Give the location of every parasitized red blood cell.
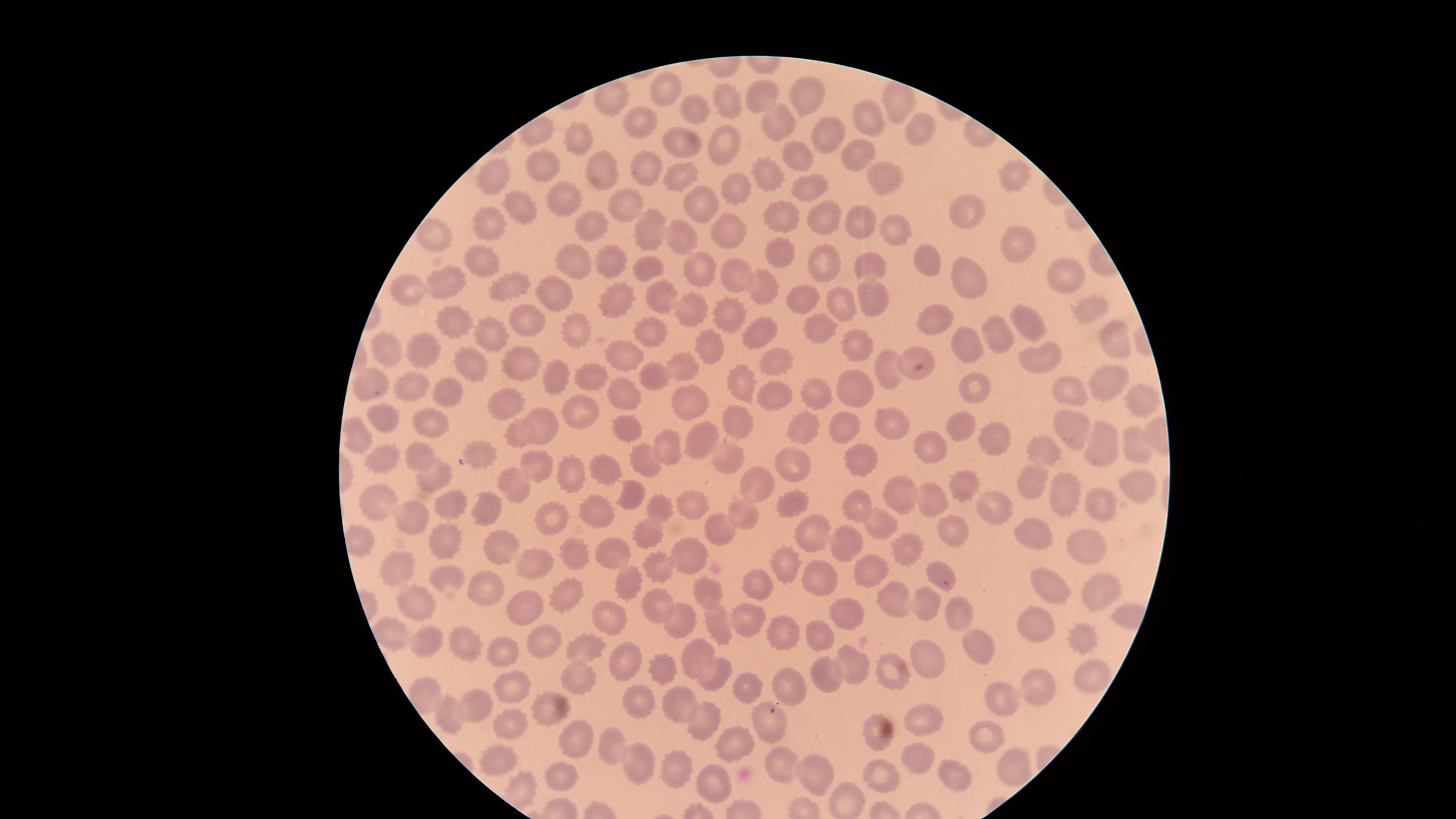
No parasitized red blood cells identified.

Approximate marker points, in pixels from the top-left corner.
Summary:
  - Uninfected red blood cells: (x=663, y=89), (x=763, y=95), (x=812, y=96), (x=726, y=101), (x=897, y=102), (x=697, y=104), (x=640, y=119), (x=869, y=119), (x=772, y=120), (x=914, y=132), (x=829, y=133), (x=683, y=137), (x=580, y=140), (x=725, y=143), (x=855, y=152), (x=795, y=157), (x=541, y=165), (x=642, y=167), (x=683, y=174), (x=491, y=176), (x=769, y=176), (x=1014, y=177), (x=603, y=178), (x=883, y=179), (x=738, y=187), (x=808, y=189), (x=560, y=196), (x=628, y=200), (x=700, y=207), (x=508, y=208), (x=783, y=212), (x=967, y=212), (x=821, y=215), (x=489, y=223), (x=896, y=224), (x=858, y=225), (x=595, y=230), (x=644, y=230), (x=727, y=231), (x=681, y=232), (x=433, y=233), (x=1018, y=249), (x=777, y=251), (x=484, y=260), (x=574, y=260), (x=927, y=262), (x=646, y=263), (x=823, y=263), (x=611, y=264), (x=874, y=266), (x=703, y=268), (x=731, y=273), (x=967, y=274), (x=1070, y=274), (x=449, y=277), (x=560, y=285), (x=762, y=285), (x=515, y=287), (x=409, y=288), (x=873, y=290), (x=661, y=293), (x=615, y=300), (x=836, y=300), (x=803, y=301), (x=1086, y=306), (x=690, y=311), (x=524, y=313), (x=731, y=313), (x=941, y=321), (x=818, y=323), (x=456, y=324), (x=576, y=324), (x=1029, y=324), (x=762, y=329), (x=650, y=330), (x=493, y=333), (x=1111, y=333), (x=998, y=334), (x=858, y=337), (x=968, y=344), (x=709, y=346), (x=394, y=350), (x=425, y=351), (x=909, y=353), (x=1036, y=354), (x=631, y=356), (x=513, y=357), (x=464, y=358), (x=775, y=361), (x=682, y=364), (x=886, y=367), (x=589, y=375), (x=650, y=376), (x=555, y=378), (x=1108, y=378), (x=742, y=381), (x=405, y=387), (x=854, y=387), (x=969, y=387), (x=771, y=388), (x=626, y=389), (x=808, y=389), (x=376, y=390), (x=1070, y=390), (x=448, y=392), (x=687, y=399), (x=500, y=403), (x=1140, y=403), (x=577, y=412), (x=740, y=417), (x=384, y=420), (x=545, y=424), (x=890, y=424), (x=432, y=425), (x=625, y=428), (x=805, y=428), (x=961, y=428), (x=1073, y=428), (x=516, y=431), (x=844, y=434), (x=359, y=436), (x=701, y=440), (x=992, y=441), (x=1136, y=443), (x=479, y=445), (x=1105, y=445), (x=934, y=449), (x=1039, y=450), (x=379, y=451), (x=667, y=451), (x=415, y=456), (x=641, y=457), (x=864, y=458), (x=729, y=459), (x=792, y=463), (x=540, y=464), (x=571, y=470), (x=605, y=470), (x=437, y=478), (x=517, y=481), (x=1034, y=482), (x=1136, y=486), (x=758, y=487), (x=960, y=488), (x=931, y=490), (x=900, y=491), (x=793, y=493), (x=631, y=494), (x=1067, y=495), (x=691, y=500), (x=374, y=501), (x=449, y=502), (x=657, y=502), (x=1104, y=502), (x=863, y=506), (x=995, y=508), (x=599, y=509), (x=493, y=511), (x=554, y=514), (x=744, y=515), (x=417, y=519), (x=883, y=522), (x=721, y=524), (x=947, y=529), (x=811, y=531), (x=1035, y=532), (x=651, y=536), (x=1085, y=538), (x=843, y=539), (x=446, y=540), (x=505, y=545), (x=910, y=548), (x=615, y=550), (x=582, y=551), (x=691, y=554), (x=784, y=561), (x=400, y=562), (x=537, y=566), (x=867, y=566), (x=658, y=568), (x=936, y=570), (x=444, y=575), (x=813, y=578), (x=629, y=582), (x=1095, y=583), (x=758, y=585), (x=486, y=588), (x=709, y=588), (x=1049, y=588), (x=568, y=591), (x=897, y=599), (x=415, y=602), (x=528, y=604), (x=919, y=605), (x=661, y=607), (x=958, y=612), (x=844, y=613), (x=612, y=616), (x=746, y=617), (x=683, y=618), (x=717, y=620), (x=1043, y=622), (x=783, y=634), (x=1075, y=634), (x=394, y=635), (x=540, y=638), (x=820, y=639), (x=423, y=642), (x=976, y=642), (x=463, y=644), (x=586, y=650), (x=502, y=653), (x=697, y=653), (x=630, y=656), (x=659, y=662), (x=852, y=665), (x=926, y=666), (x=1092, y=670), (x=893, y=677), (x=717, y=678), (x=828, y=678), (x=573, y=681), (x=513, y=684), (x=787, y=685), (x=753, y=687), (x=1038, y=687), (x=429, y=694), (x=634, y=701), (x=674, y=702), (x=996, y=702), (x=474, y=707), (x=553, y=709), (x=451, y=713), (x=706, y=720), (x=925, y=720), (x=507, y=722), (x=765, y=724), (x=872, y=724), (x=989, y=733), (x=570, y=736), (x=734, y=741), (x=613, y=748), (x=494, y=759), (x=785, y=759), (x=1007, y=759), (x=919, y=760), (x=636, y=763), (x=674, y=763), (x=565, y=775), (x=948, y=775), (x=882, y=777), (x=820, y=778), (x=718, y=783), (x=848, y=798)
  - Field of view: single
  - Capture: smartphone photograph through the microscope eyepiece
  - Preparation: thin blood smear
  - Stain: Giemsa
  - Image size: 1456×819 pixels
  - Visible region: circular